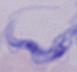

modality = micrograph
magnification = 1000x
identification = trypanosome